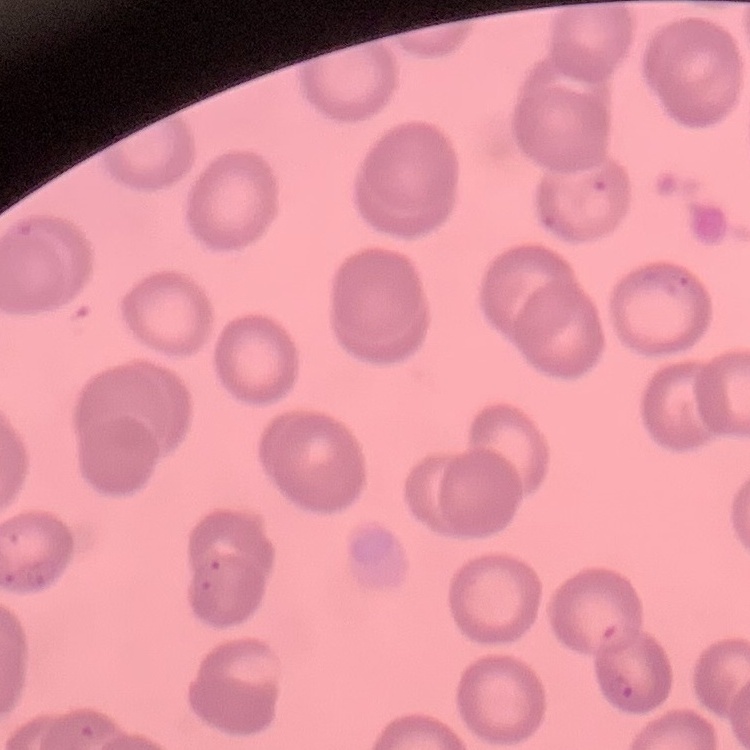

Summary:
  - Red blood cell morphology: no rouleaux formation
  - Image type: square crop of a larger photomicrograph
  - Preparation: thin blood film
  - Stain: Field's or Giemsa